Assess this cell for malaria.
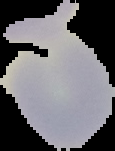
It is uninfected.

Cell region segmented out of the field of view; the surrounding area is masked to black. Image is 115×151 pixels. From a thin blood smear.